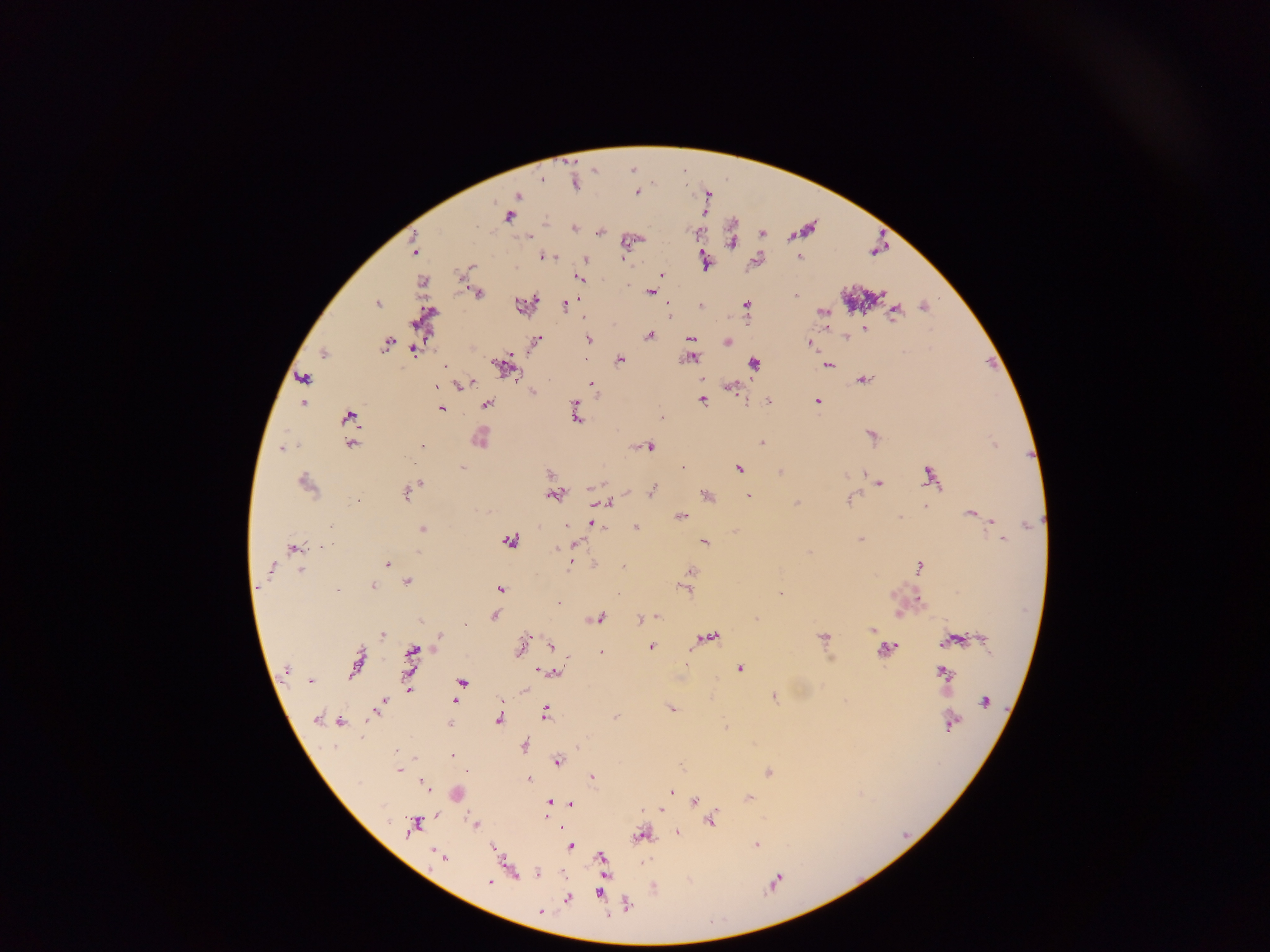

country = Ghana
Plasmodium parasite locations = approximate centers as x y in pixels: 634 168; 544 178; 652 181; 576 182; 638 190; 708 194; 519 195; 511 216; 734 224; 576 225; 805 228; 601 230; 699 231; 763 232; 733 235; 632 238; 733 239; 415 247; 878 247; 545 255; 801 256; 587 257; 758 259; 706 260; 468 268; 663 273; 580 278; 423 281; 651 289; 477 291; 797 293; 861 295; 379 301; 528 302; 566 304; 670 304; 702 304; 926 304; 747 305; 895 311; 825 312; 427 316; 866 328; 651 333; 847 336; 589 337; 692 337; 728 340; 537 341; 389 342; 812 342; 692 344; 325 350; 415 350; 691 355; 621 358; 755 362; 992 362; 507 363; 829 364; 446 366; 305 377; 864 378; 468 383; 593 385; 438 386; 732 386; 534 390; 704 400; 769 400; 820 400; 304 402; 488 404; 443 409; 577 412; 351 415; 662 415; 873 433; 481 437; 763 441; 352 443; 995 443; 647 444; 423 445; 283 446; 685 465; 463 466; 740 467; 781 470; 550 471; 865 473; 931 473; 307 480; 421 482; 879 482; 414 486; 653 489; 408 490; 555 493; 708 493; 750 495; 853 498; 607 501; 798 502; 926 505; 972 511; 681 514; 900 517; 991 520; 592 521; 637 526; 424 528; 862 537; 1004 538; 512 539; 705 540; 575 543; 294 546; 574 562; 388 563; 594 563; 921 564; 623 566; 692 571; 409 580; 689 581; 375 584; 688 587; 502 588; 339 589; 782 591; 919 598; 901 612; 496 614; 656 614; 600 616; 640 617; 465 623; 875 630; 384 633; 440 635; 709 636; 826 636; 552 646; 653 646; 888 647; 522 648; 414 649; 602 650; 568 658; 357 666; 741 667; 944 671; 554 672; 463 681; 525 687; 409 689; 775 695; 502 700; 383 701; 455 701; 672 707; 546 711; 618 716; 500 718; 341 720; 450 723; 726 724; 526 744; 578 745; 399 749; 453 754; 415 755; 559 759; 682 765; 469 767; 400 769; 769 771; 593 774; 529 777; 426 785; 673 788; 458 793; 749 795; 551 800; 696 800; 555 801; 571 803; 661 808; 437 814; 546 816; 712 820; 477 822; 418 823; 678 831; 644 833; 757 843; 496 845; 572 846; 443 856; 602 856; 513 870; 538 871; 607 876; 777 879; 492 881; 654 886; 601 894; 569 897; 627 903; 542 910
capture = mobile-phone photograph through a microscope
image size = 1270×952 pixels
preparation = thick blood film
field of view = single